Locate every parasitized RBC.
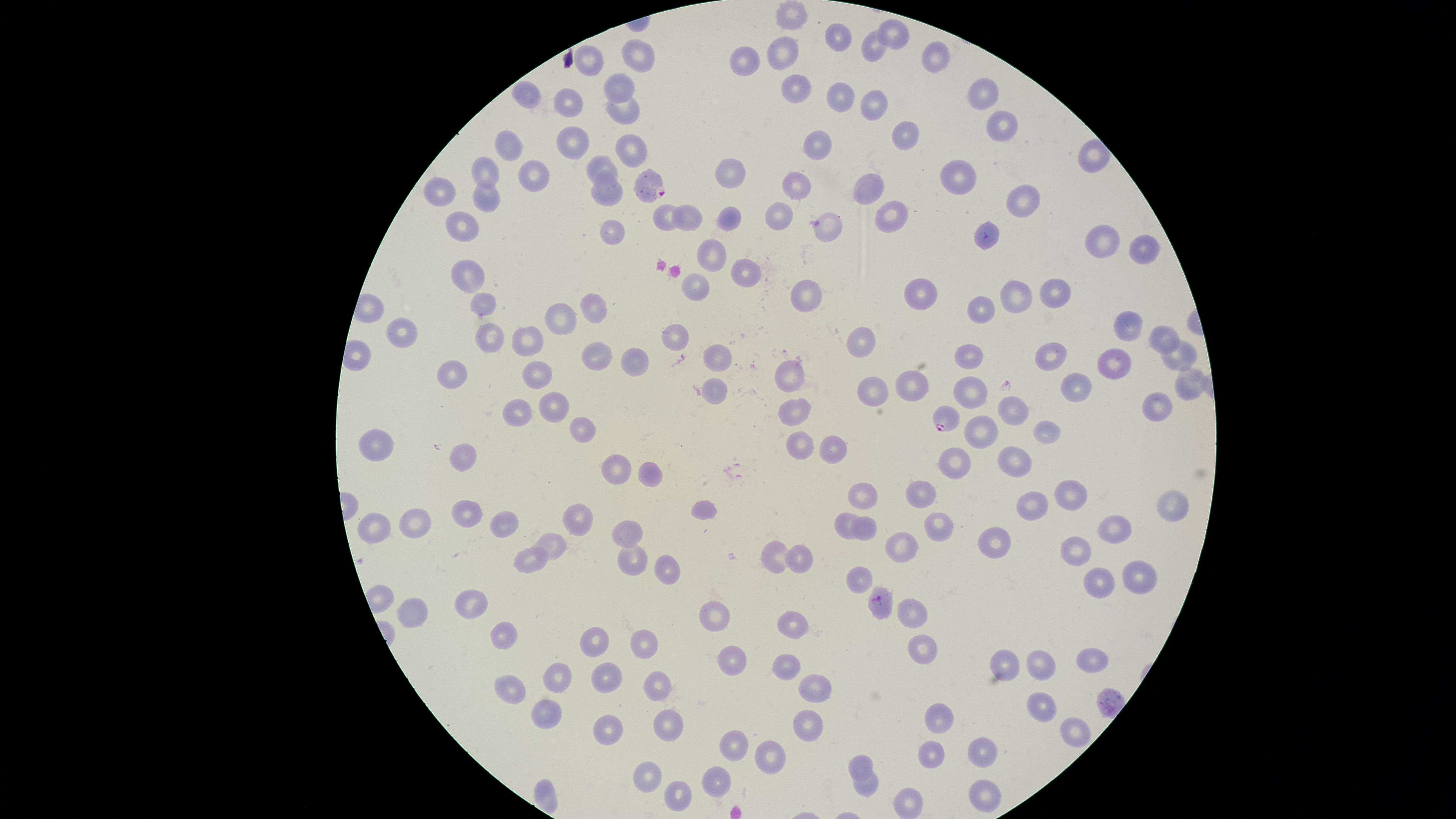

Approximate marker points as [x, y] in pixels.
Parasitized RBCs: [648, 187], [945, 420], [876, 600].

Approximate marker points as [x, y] in pixels.
Summary:
  - Uninfected RBCs: [791, 15], [892, 33], [837, 34], [869, 48], [784, 49], [932, 57], [638, 59], [746, 60], [590, 65], [618, 84], [794, 89], [980, 92], [523, 97], [838, 98], [868, 102], [570, 106], [623, 110], [1000, 126], [905, 134], [574, 141], [819, 144], [509, 149], [628, 149], [1090, 150], [486, 170], [600, 170], [730, 172], [539, 179], [962, 179], [798, 186], [867, 189], [440, 193], [604, 193], [486, 196], [1024, 202], [888, 212], [780, 214], [660, 216], [726, 216], [691, 221], [826, 227], [608, 229], [465, 230], [983, 238], [1098, 243], [1140, 248], [708, 255], [743, 269], [469, 276], [691, 285], [1014, 294], [1052, 294], [928, 295], [802, 297], [593, 307], [485, 310], [983, 310], [557, 322], [1119, 327], [406, 331], [530, 338], [859, 338], [681, 339], [1154, 339], [492, 346], [600, 356], [713, 356], [967, 356], [1175, 356], [1051, 359], [639, 360], [1111, 368], [536, 374], [795, 374], [454, 379], [911, 380], [1184, 383], [1073, 387], [712, 388], [975, 390], [872, 393], [1156, 402], [550, 406], [1013, 408], [794, 410], [512, 414], [577, 428], [979, 431], [1046, 431], [381, 443], [800, 445], [828, 446], [1012, 456], [459, 457], [954, 462], [612, 468], [651, 476], [922, 491], [867, 496], [1071, 496], [1173, 503], [1034, 506], [705, 510], [467, 512], [504, 517], [578, 517], [842, 519], [418, 522], [1113, 524], [934, 525], [867, 526], [374, 530], [626, 530], [902, 543], [999, 544], [551, 547], [1075, 547], [633, 556], [804, 556], [773, 557], [528, 561], [666, 568], [1135, 575], [862, 580], [1095, 581], [472, 604], [914, 606], [414, 607], [713, 614], [792, 625], [501, 633], [596, 641], [647, 646], [921, 646], [734, 656], [1088, 659], [1005, 662], [784, 665], [1042, 665], [608, 677], [558, 681], [659, 682], [513, 687], [817, 689], [1041, 701], [548, 710], [945, 718], [669, 721], [808, 725], [1072, 727], [605, 730], [987, 748], [734, 749], [928, 757], [771, 758], [866, 763], [651, 769], [714, 783], [868, 786], [680, 794], [981, 797], [909, 805]
  - Species: Plasmodium falciparum
  - Field of view: single
  - Stain: Giemsa
  - Image size: 1456×819 pixels
  - Capture: smartphone photograph through the microscope eyepiece
  - Preparation: thin smear of blood
  - Visible region: circular